State which parasite is depicted.
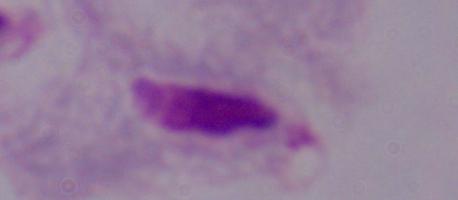

This is a trichomonad.

Summary:
  - Magnification: 1000x
  - Modality: photomicrograph